Describe the morphology of the red blood cells.
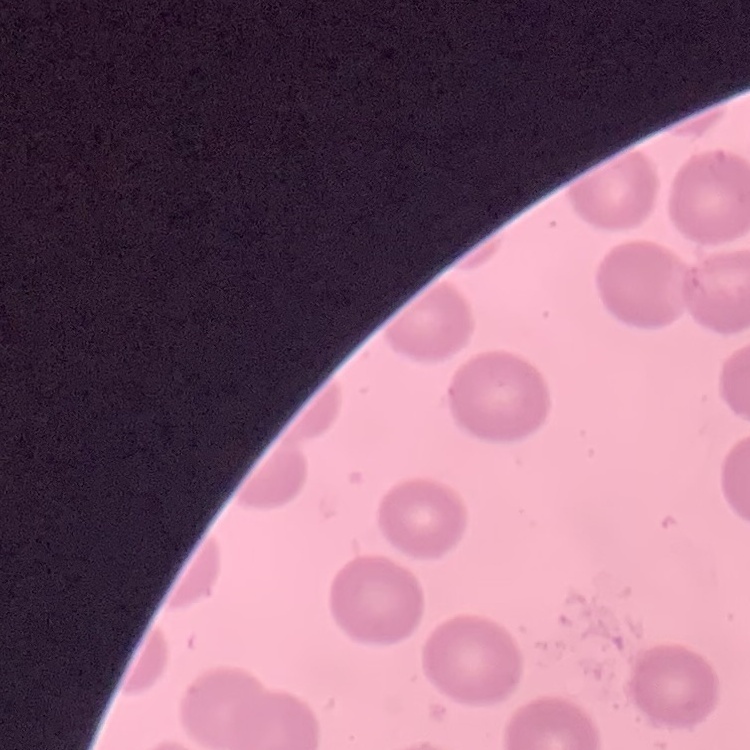
No rouleaux formation.

Field's or Giemsa stain. Square crop of a larger photomicrograph. Thin blood smear.